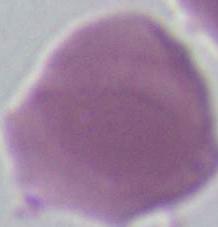
1000x magnification. An erythrocyte is seen. Photomicrograph.